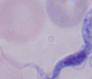 Micrograph. A trypanosome is shown. 1000x magnification.